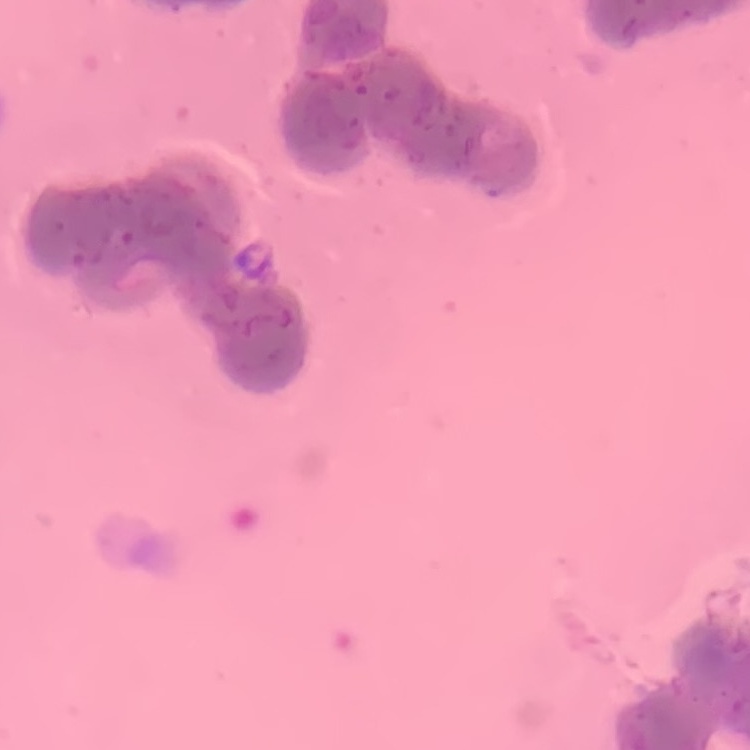

red_blood_cell_morphology: rouleaux formation
stain: Field's or Giemsa
preparation: thin blood film
image_type: one tile cut from a larger photomicrograph